Describe the morphology of the erythrocytes.
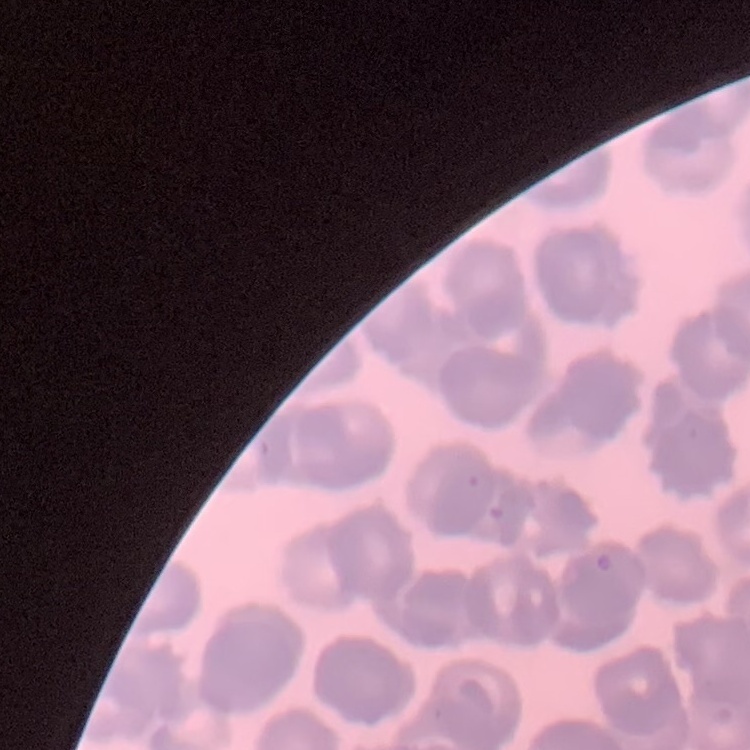
They show rouleaux formation.

Summary:
  - Stain: Field's or Giemsa
  - Image type: square crop of a larger photomicrograph
  - Preparation: thin blood film